Locate every Plasmodium vivax-infected red blood cell.
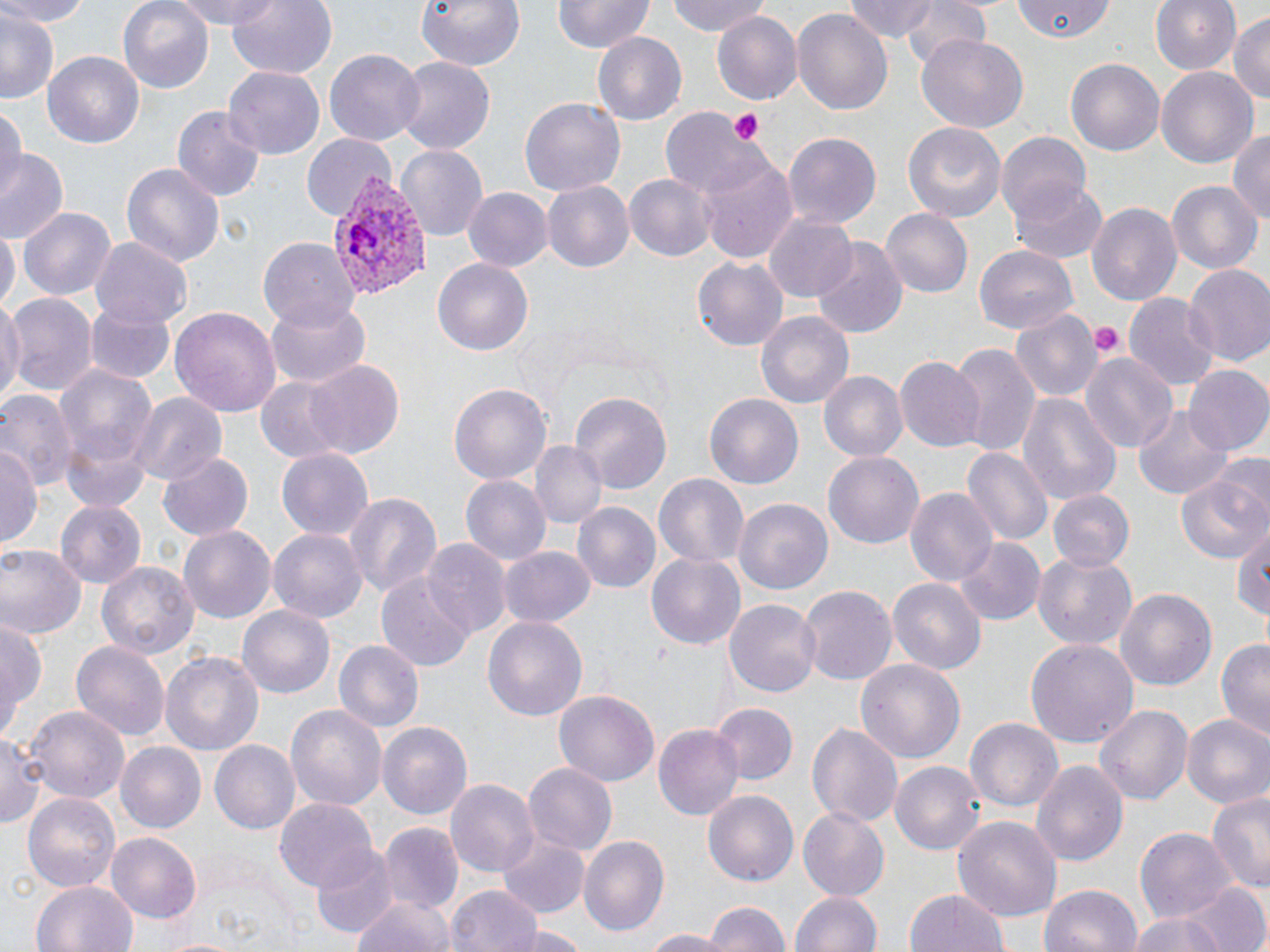

Approximate bounding boxes as [x1, y1, x2, y2] in pixels.
Plasmodium vivax-infected red blood cells: [328, 179, 429, 300].

Summary:
  - Uninfected red blood cell locations: [0, 0, 95, 25], [118, 0, 212, 91], [179, 0, 280, 31], [224, 0, 337, 81], [416, 0, 526, 71], [667, 0, 771, 37], [843, 0, 945, 44], [900, 0, 993, 70], [1150, 0, 1241, 76], [551, 1, 652, 55], [1013, 1, 1118, 43], [790, 7, 893, 114], [0, 11, 58, 104], [711, 12, 801, 107], [1229, 13, 1270, 109], [593, 31, 687, 123], [916, 34, 1027, 132], [324, 49, 425, 145], [44, 50, 147, 149], [394, 57, 496, 156], [1066, 58, 1165, 158], [225, 67, 326, 158], [1155, 67, 1260, 168], [519, 97, 626, 197], [0, 104, 23, 204], [171, 105, 267, 202], [660, 107, 764, 197], [901, 122, 1007, 223], [1228, 128, 1270, 227], [995, 131, 1092, 227], [301, 133, 395, 222], [783, 133, 880, 230], [394, 144, 488, 240], [0, 152, 68, 242], [696, 154, 798, 262], [121, 162, 226, 270], [625, 172, 717, 262], [1009, 180, 1108, 264], [1167, 180, 1261, 276], [544, 181, 633, 274], [464, 187, 552, 272], [1087, 201, 1182, 307], [19, 206, 116, 300], [881, 208, 973, 298], [766, 212, 859, 302], [0, 223, 18, 311], [91, 238, 190, 326], [257, 238, 359, 331], [810, 238, 909, 337], [976, 245, 1079, 335], [692, 256, 788, 351], [432, 257, 533, 356], [1183, 264, 1270, 368], [5, 293, 96, 399], [1123, 294, 1220, 391], [263, 296, 371, 389], [0, 297, 23, 407], [85, 303, 176, 384], [170, 305, 281, 417], [1010, 310, 1103, 407], [756, 312, 853, 412], [948, 343, 1038, 458], [1081, 352, 1177, 456], [895, 356, 983, 450], [51, 358, 159, 490], [305, 359, 404, 459], [1183, 366, 1270, 456], [819, 371, 907, 464], [254, 374, 359, 464], [448, 383, 551, 487], [0, 389, 77, 493], [132, 392, 225, 487], [706, 392, 803, 491], [571, 393, 671, 493], [1017, 393, 1120, 507], [1134, 405, 1231, 500], [530, 440, 606, 531], [0, 441, 40, 546], [962, 446, 1051, 546], [275, 448, 374, 540], [824, 450, 926, 550], [157, 451, 253, 542], [1177, 465, 1269, 563], [654, 472, 749, 570], [461, 476, 552, 566], [904, 487, 999, 588], [1047, 490, 1133, 573], [344, 491, 441, 602], [735, 499, 833, 593], [56, 500, 146, 587], [573, 502, 661, 595], [1233, 525, 1270, 627], [179, 526, 275, 623], [268, 526, 367, 623], [952, 537, 1045, 626], [422, 539, 512, 635], [0, 544, 85, 640], [501, 545, 595, 627], [1032, 550, 1137, 651], [645, 551, 746, 650], [100, 562, 198, 663], [377, 574, 475, 672], [888, 577, 988, 674], [799, 586, 895, 684], [1116, 587, 1217, 692], [725, 598, 821, 698], [238, 606, 334, 697], [0, 612, 43, 740], [482, 614, 587, 718], [1215, 637, 1270, 743], [1027, 638, 1137, 749], [332, 639, 424, 736], [70, 640, 170, 741], [161, 652, 262, 756], [856, 658, 965, 768], [556, 691, 658, 788], [712, 703, 798, 786], [287, 704, 385, 813], [1093, 704, 1196, 806], [25, 705, 132, 805], [1182, 714, 1270, 807], [964, 717, 1062, 814], [806, 718, 903, 829], [377, 721, 472, 822], [655, 723, 745, 820], [1, 726, 44, 831], [211, 740, 303, 834], [116, 741, 205, 833], [1030, 758, 1129, 867], [891, 763, 983, 853], [524, 764, 616, 853], [447, 779, 539, 878], [1206, 789, 1270, 896], [22, 790, 120, 891], [704, 792, 798, 885], [274, 796, 379, 894], [799, 807, 891, 900], [953, 816, 1061, 926], [378, 824, 464, 917], [1135, 827, 1235, 924], [106, 832, 202, 924], [500, 832, 589, 915], [580, 836, 670, 937], [310, 846, 398, 938], [30, 880, 135, 952], [1185, 882, 1269, 952], [1039, 883, 1144, 952], [446, 885, 545, 952], [790, 890, 883, 952], [909, 890, 1010, 952], [349, 895, 454, 952], [700, 900, 788, 952], [1126, 906, 1241, 952], [513, 924, 589, 952], [633, 929, 737, 950], [153, 934, 251, 952]
  - Platelet locations: [728, 108, 767, 145], [1090, 323, 1125, 356]
  - Slide-level diagnosis: Plasmodium vivax
  - Image size: 1270×952 pixels
  - Stain: May-Grünwald-Giemsa
  - Field of view: single
  - Magnification: 1000x
  - Modality: optical microscopy
  - Preparation: thin blood smear